Point out each Plasmodium parasite.
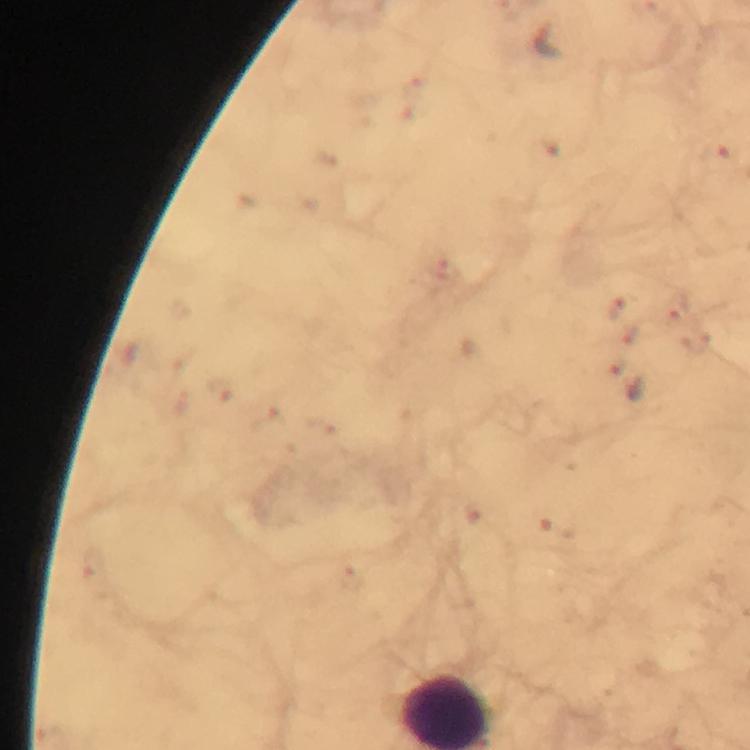

Approximate centers as {x, y} in pixels.
Plasmodium parasites: {548, 43}, {718, 158}, {441, 269}, {676, 306}, {624, 308}, {639, 334}, {694, 342}, {627, 382}, {219, 390}, {472, 513}, {557, 527}, {93, 564}, {352, 577}.

preparation: thick smear
image_size: 750×750 pixels
magnification: 100x
context: from a malaria diagnostic workup
capture: smartphone photograph through a microscope
immersion_oil: applied
stain: Giemsa
cropped_from: one field of view